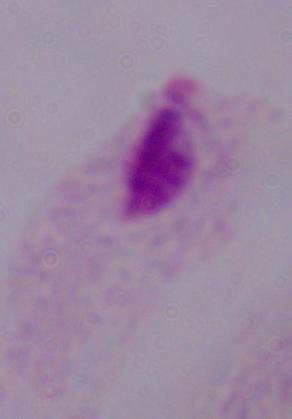 A trichomonad is seen. Captured at 1000x magnification. Micrograph.